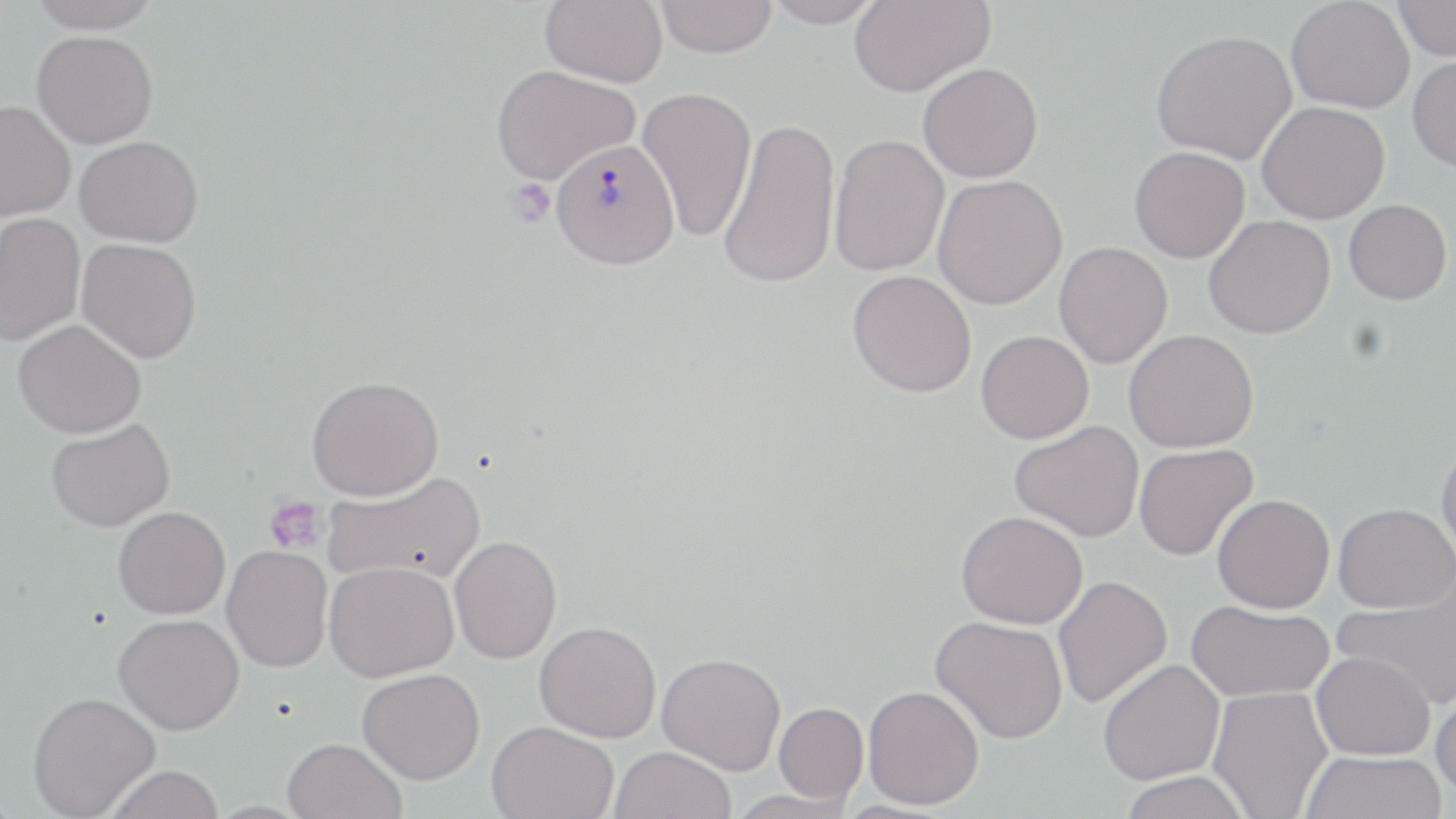

slide-level diagnosis = Plasmodium vivax
stain = May-Grünwald-Giemsa
modality = light microscopy
magnification = 1000x
platelet locations = approximate bounding boxes as (x1,y1)-(x2,y2) corner pairs in pixels: (506,180)-(556,228), (264,495)-(326,553)
uninfected red blood cell locations = approximate bounding boxes as (x1,y1)-(x2,y2) corner pairs in pixels: (28,0)-(163,33), (540,0)-(668,87), (656,0)-(777,57), (763,0)-(883,27), (849,0)-(995,98), (1285,0)-(1415,114), (1393,0)-(1456,61), (1151,29)-(1297,165), (32,31)-(158,148), (1408,55)-(1456,172), (918,63)-(1043,182), (491,64)-(640,184), (636,86)-(757,242), (0,100)-(76,221), (1257,101)-(1389,224), (717,116)-(841,290), (828,133)-(950,277), (75,135)-(204,247), (1129,146)-(1250,263), (932,174)-(1067,309), (1344,199)-(1452,304), (0,213)-(85,346), (1203,214)-(1335,339), (77,239)-(201,363), (1054,242)-(1173,368), (847,270)-(977,397), (13,320)-(145,438), (1124,329)-(1259,453), (976,330)-(1094,444), (306,375)-(444,501), (45,418)-(174,531), (1010,420)-(1145,542), (1436,438)-(1456,562), (1134,443)-(1258,561), (322,470)-(485,586), (1212,494)-(1335,612), (1333,502)-(1456,612), (113,506)-(230,619), (956,509)-(1088,629), (449,535)-(562,664), (222,545)-(333,672), (324,561)-(459,682), (1052,575)-(1172,708), (1333,575)-(1455,706), (1186,600)-(1334,703), (113,613)-(244,735), (931,615)-(1068,744), (534,620)-(661,742), (1311,651)-(1436,760), (657,652)-(786,774), (1098,659)-(1225,785), (358,668)-(485,784), (1432,683)-(1456,802), (862,685)-(984,810), (1208,686)-(1333,818), (27,691)-(160,818), (773,702)-(868,803), (486,720)-(618,818), (282,737)-(407,819), (610,746)-(736,819), (1299,751)-(1447,819), (103,765)-(225,819), (1118,771)-(1252,819), (723,789)-(860,818)
preparation = thin blood film
image size = 1456×819 pixels
Plasmodium vivax-infected red blood cell locations = approximate bounding boxes as (x1,y1)-(x2,y2) corner pairs in pixels: (552,137)-(680,269)
field of view = single